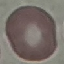 Result: no malaria parasites seen. Automatically extracted cell patch, resized to 64 × 64 pixels. Giemsa stain. Photographed with a smartphone camera at the microscope eyepiece. Thin blood film.